Locate the Plasmodium falciparum-infected red blood cells and any of indeterminate infection status.
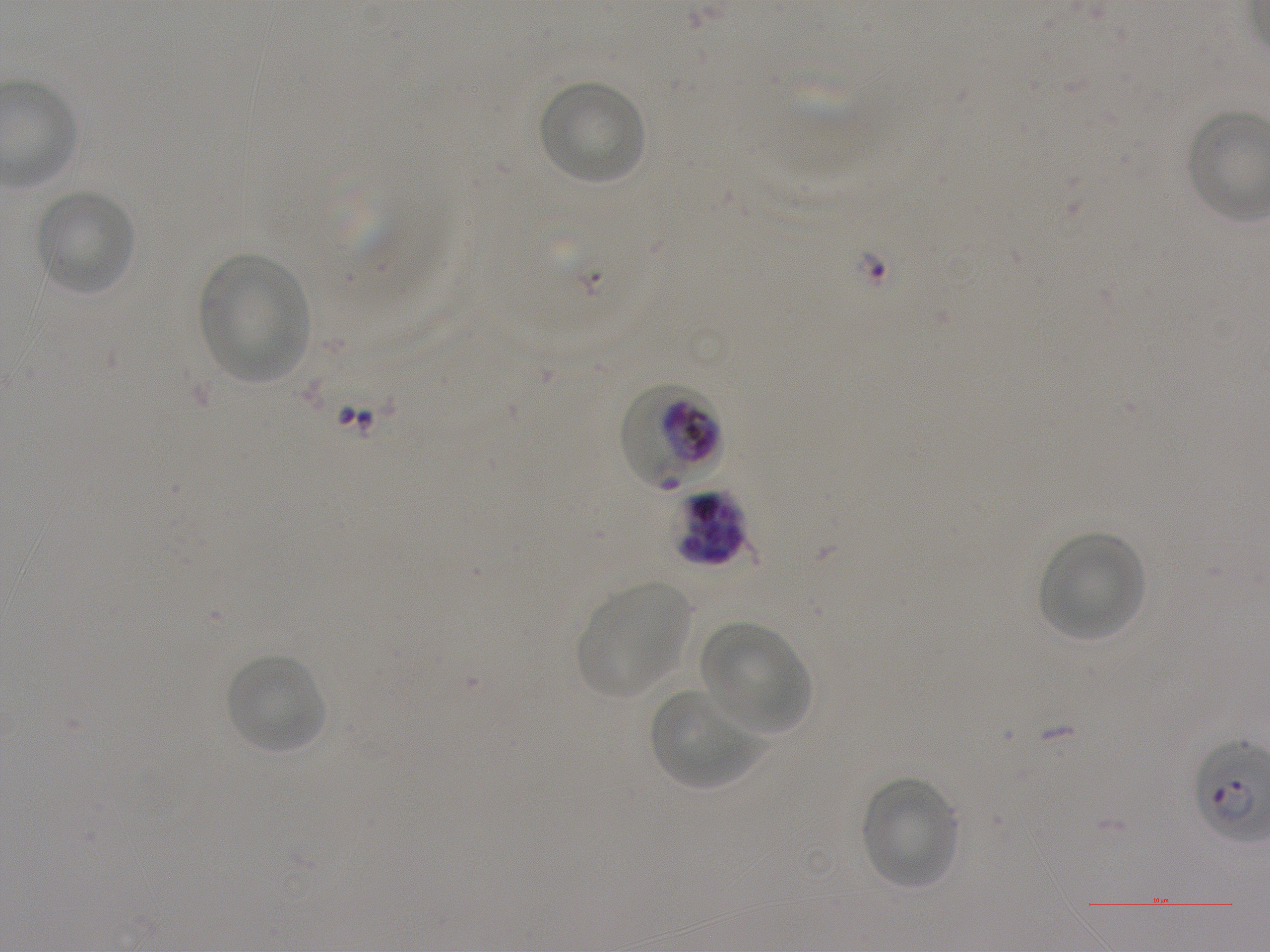

Approximate bounding rectangles given as corner coordinates in pixels from the top-left. Not every red blood cell is marked. A life-cycle stage — or a range of stages, where the recorded stages span more than one — follows each staged infected red blood cell.
Infected red blood cells: (x1=672, y1=489, x2=749, y2=568) schizont.
Red blood cells of indeterminate infection status: (x1=621, y1=384, x2=721, y2=492).

locations of uninfected red blood cells = (x1=539, y1=81, x2=646, y2=185), (x1=34, y1=189, x2=137, y2=296), (x1=200, y1=254, x2=311, y2=384), (x1=1038, y1=532, x2=1146, y2=642), (x1=577, y1=584, x2=691, y2=698), (x1=701, y1=623, x2=809, y2=735), (x1=225, y1=653, x2=328, y2=754), (x1=650, y1=689, x2=760, y2=790), (x1=859, y1=775, x2=958, y2=891)
objective = 100x, oil immersion, numerical aperture 1.25
image size = 1270×952 pixels
donor blood group = A+
preparation = thin blood film
stain = Giemsa
field of view = one from this slide
culture = Plasmodium falciparum strain NF54, static, in vitro